Identify the parasite.
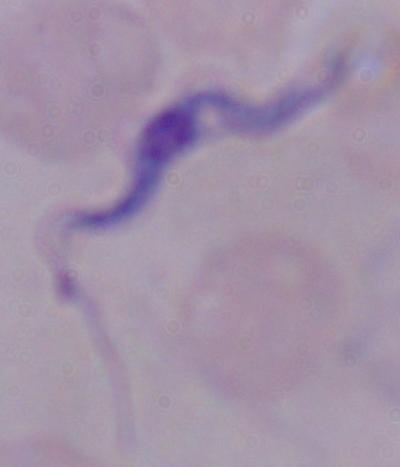
A trypanosome.

1000x magnification. Micrograph.